Assess this cell for malaria.
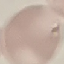

It is uninfected.

preparation: thin smear
stain: Giemsa
capture: smartphone through the microscope eyepiece
image_type: cell patch, automatically extracted from a larger field of view and resized to 64 × 64 pixels